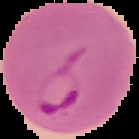
Image is 139×139 pixels. From a thin blood smear. Malaria status: parasitized. The area outside the segmented cell region is set to black.